Comment on the morphology of the red blood cells.
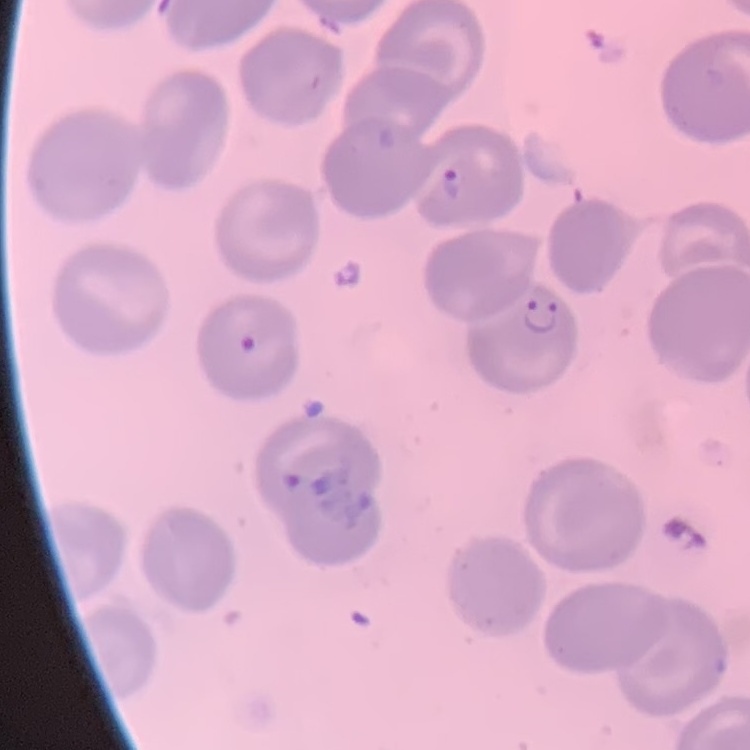
They show no rouleaux formation.

preparation: thin blood film
image_type: square crop of a larger photomicrograph
stain: Field's or Giemsa